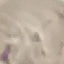

{
  "malaria_status": "uninfected",
  "preparation": "thin blood film",
  "image_type": "cell patch, automatically extracted from a larger field of view and resized to 64 × 64 pixels",
  "capture": "smartphone through the microscope eyepiece",
  "stain": "Giemsa"
}